Name the parasite shown.
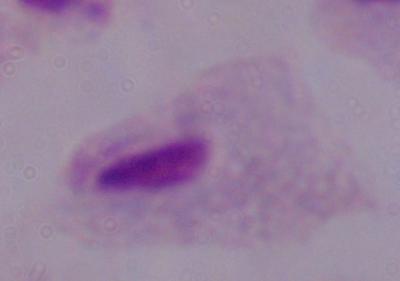
This is a trichomonad.

1000x magnification. Photomicrograph.